Point out Plasmodium parasites and leukocytes.
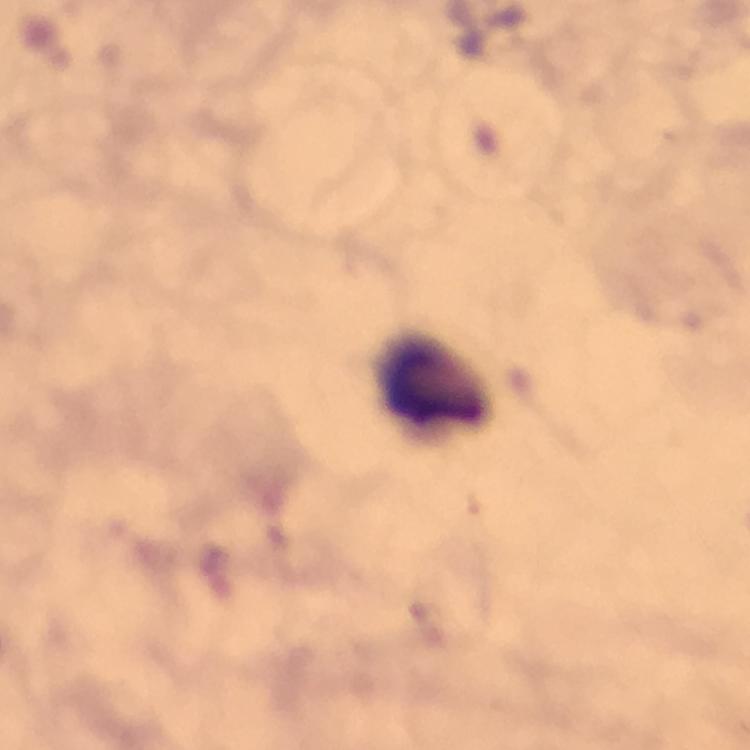
No Plasmodium parasites detected.
Approximate object centers, in pixels from the top-left corner.
Leukocytes: (x=435, y=381).

magnification = 100x
capture = smartphone photograph through a microscope
preparation = thick blood smear
image size = 750×750 pixels
cropped from = a single field of view
stain = Giemsa
context = from a diagnostic examination for malaria
immersion oil = used